Classify this cell by malaria status.
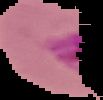
Parasitized.

The area outside the segmented cell region is set to black. From a thin blood film. Image is 103×100 pixels.